State which parasite is depicted.
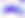

This is Toxoplasma gondii.

{
  "magnification": "400x",
  "modality": "photomicrograph"
}